Give the position of every Plasmodium parasite.
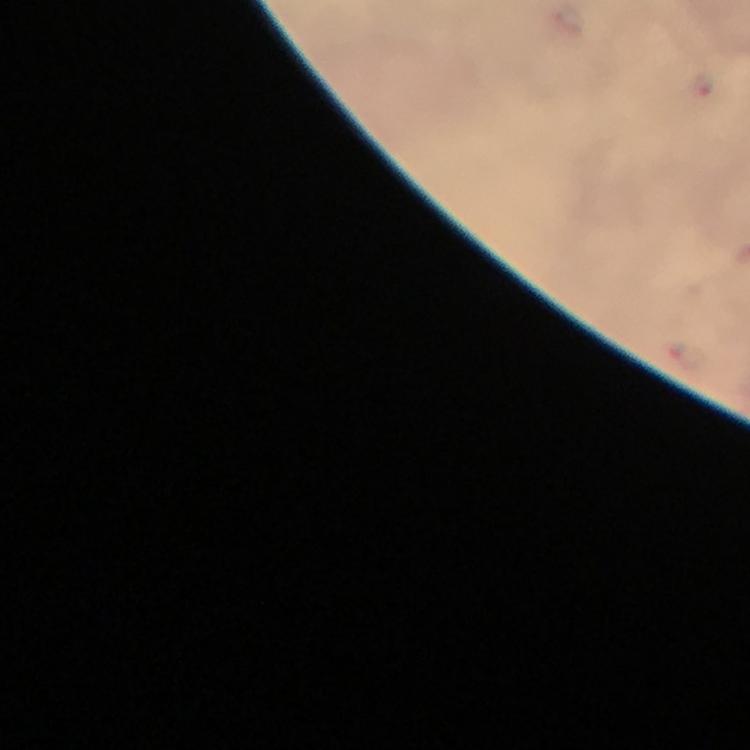
Approximate centers as [x, y] in pixels.
Plasmodium parasites: [702, 85].

Summary:
  - Capture: smartphone mounted on the microscope
  - Stain: Giemsa
  - Image size: 750×750 pixels
  - Immersion oil: applied
  - Context: from a diagnostic examination for malaria
  - Preparation: thick smear
  - Cropped from: one field of view
  - Magnification: 100x